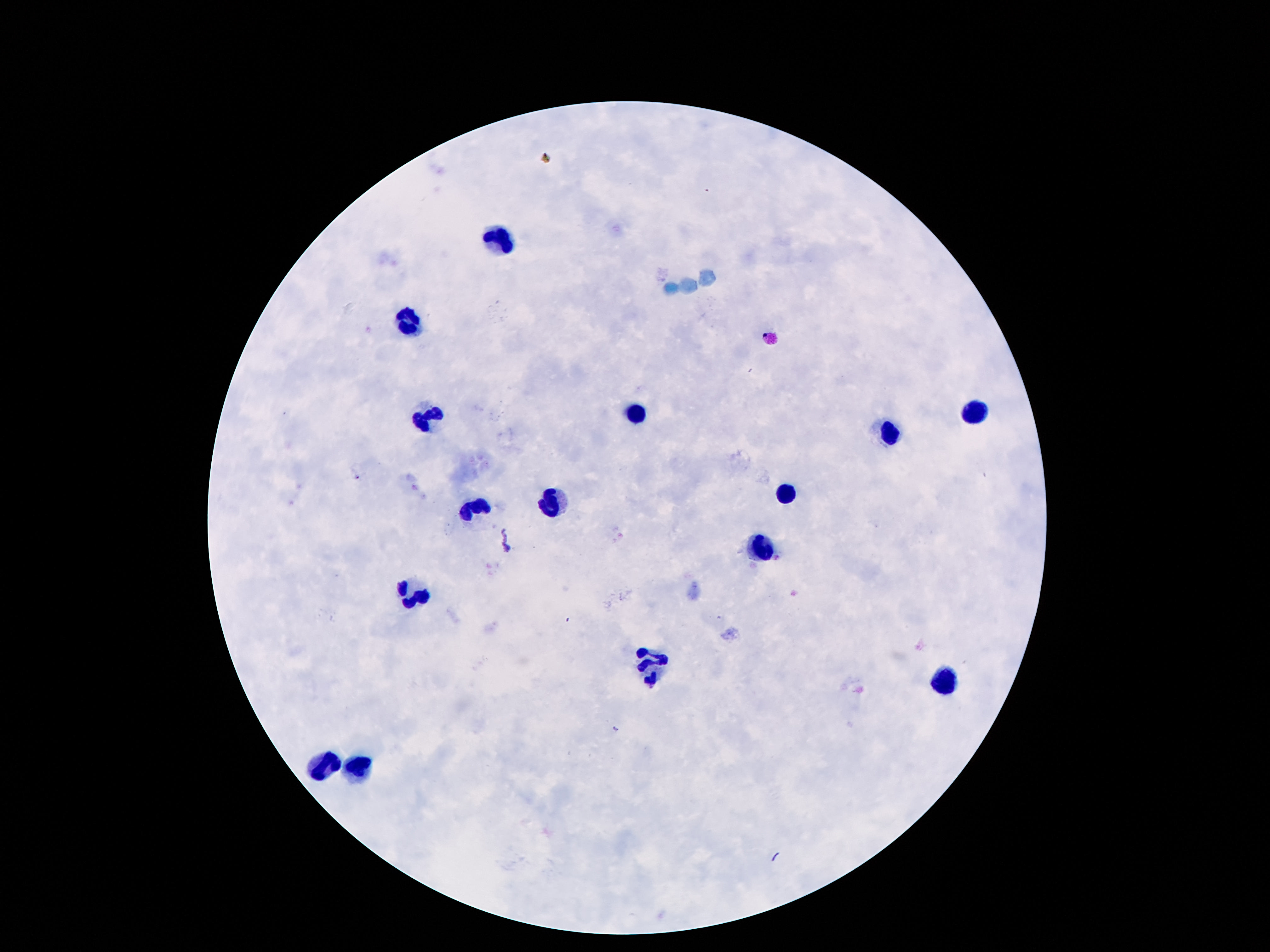

Approximate centers as {x, y} in pixels. Leukocyte locations: {497, 239}, {405, 321}, {637, 413}, {973, 413}, {427, 418}, {887, 434}, {785, 493}, {551, 504}, {473, 509}, {757, 546}, {411, 591}, {651, 665}, {942, 684}, {324, 765}, {356, 768}. 100x magnification. Patient malaria status: uninfected. Photographed through the microscope eyepiece with a smartphone camera. Image is 1270×952 pixels. Thick blood smear. Giemsa stain. Single field of view.